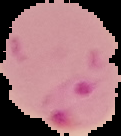
Summary:
  - Malaria status: parasitized
  - Image type: cell region segmented out of the field of view; surrounding area masked to black
  - Image size: 121×136 pixels
  - Preparation: thin blood smear